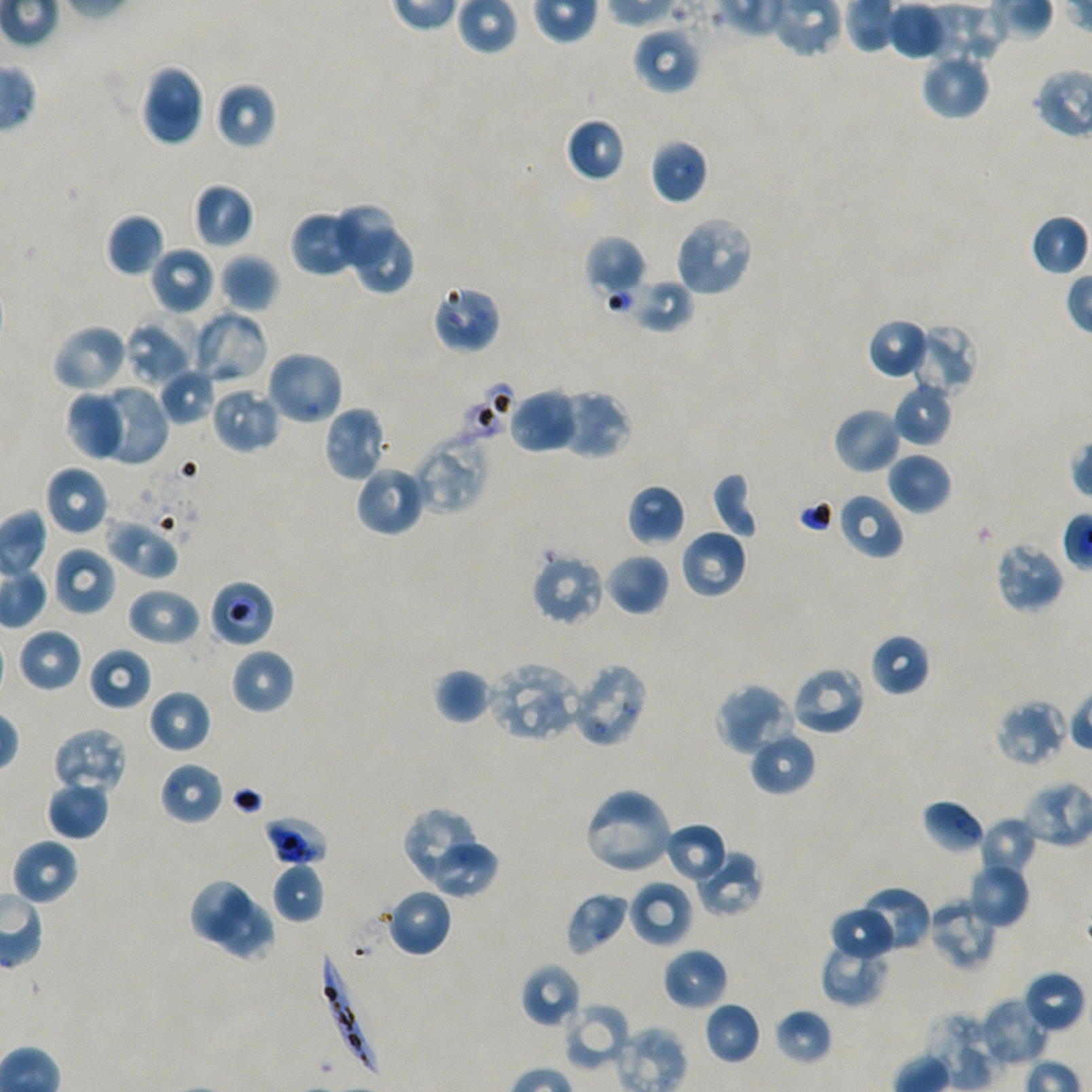
Approximate bounding boxes as {x1, y1, x2, y2} in pixels. Not every red blood cell is marked.
Summary:
  - Locations of red blood cells of indeterminate infection status: {432, 283, 501, 354}, {456, 380, 516, 444}, {209, 579, 275, 648}, {262, 816, 329, 867}
  - Locations of uninfected red blood cells: {887, 0, 947, 60}, {633, 26, 702, 94}, {920, 51, 990, 120}, {139, 64, 204, 147}, {215, 81, 277, 149}, {564, 117, 626, 183}, {650, 139, 708, 204}, {193, 183, 255, 249}, {335, 202, 395, 270}, {105, 213, 166, 278}, {673, 215, 754, 297}, {293, 216, 352, 274}, {354, 228, 415, 295}, {584, 235, 647, 299}, {150, 246, 216, 316}, {219, 253, 279, 313}, {629, 278, 695, 335}, {192, 310, 270, 388}, {124, 314, 201, 388}, {867, 317, 928, 379}, {911, 322, 979, 395}, {52, 323, 131, 394}, {266, 350, 344, 426}, {158, 368, 217, 426}, {892, 380, 953, 448}, {91, 385, 168, 465}, {211, 386, 281, 454}, {509, 388, 579, 454}, {64, 390, 128, 460}, {555, 390, 632, 459}, {322, 405, 387, 483}, {833, 407, 903, 474}, {413, 431, 490, 514}, {886, 452, 951, 515}, {354, 463, 426, 537}, {44, 465, 110, 536}, {710, 473, 759, 539}, {626, 484, 685, 545}, {837, 492, 904, 560}, {105, 519, 179, 579}, {680, 528, 748, 598}, {994, 540, 1066, 615}, {52, 547, 115, 616}, {603, 551, 669, 617}, {530, 553, 605, 627}, {127, 587, 201, 647}, {18, 628, 84, 693}, {869, 633, 931, 697}, {88, 647, 152, 710}, {230, 648, 295, 715}, {568, 661, 649, 748}, {488, 662, 582, 743}, {789, 665, 867, 737}, {434, 668, 490, 725}, {714, 682, 794, 756}, {147, 689, 211, 754}, {994, 698, 1071, 767}, {51, 727, 128, 795}, {749, 731, 816, 796}, {159, 761, 224, 825}, {46, 780, 110, 840}, {582, 787, 674, 876}, {922, 798, 985, 855}, {400, 807, 476, 880}, {979, 816, 1039, 879}, {664, 823, 728, 884}, {11, 839, 79, 906}, {431, 844, 500, 899}, {692, 850, 763, 917}, {966, 861, 1030, 928}, {272, 862, 326, 924}, {187, 877, 249, 941}, {629, 879, 693, 949}, {854, 886, 930, 954}, {386, 888, 452, 958}, {566, 892, 630, 957}, {926, 896, 998, 972}, {216, 899, 275, 962}, {829, 906, 896, 962}, {820, 939, 889, 1006}, {662, 947, 728, 1011}, {520, 962, 582, 1030}, {1021, 970, 1085, 1035}, {978, 995, 1051, 1068}, {564, 1001, 632, 1071}, {704, 1002, 762, 1065}, {774, 1007, 833, 1066}, {928, 1011, 998, 1090}, {617, 1025, 687, 1092}
  - Locations of infected red blood cells: {317, 946, 381, 1078}
  - Preparation: thin blood film
  - Objective: 100x, oil immersion, numerical aperture 1.45
  - Image size: 1092×1092 pixels
  - Donor blood group: A+/O+
  - Stain: Giemsa
  - Field of view: one from this slide
  - Culture: static in-vitro P. falciparum strain NF54